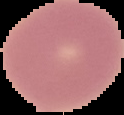

preparation: thin blood film
image_type: cell region segmented out of the field of view; surrounding area masked to black
image_size: 124×115 pixels
malaria_status: uninfected